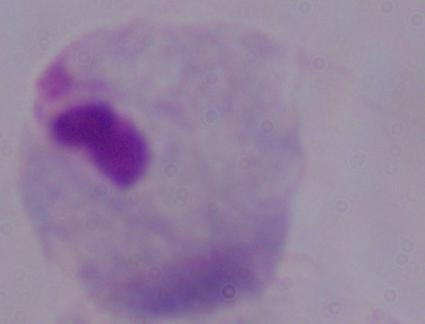
magnification = 1000x
modality = micrograph
identification = trichomonad